State the blood parasite species.
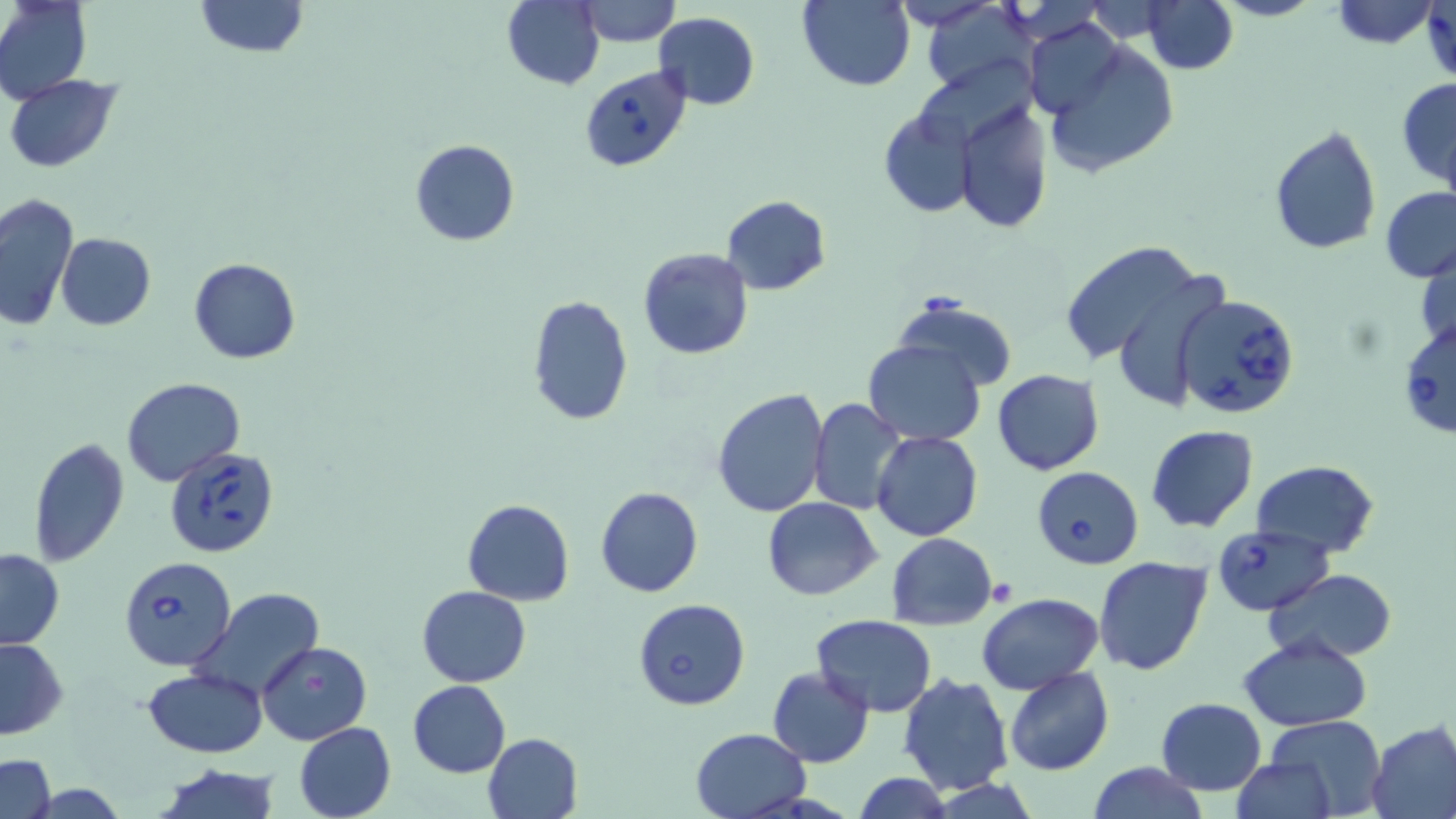

Babesia divergens.

Approximate bounding boxes as [x1, y1, x2, y2] in pixels. Uninfected red blood cell locations: [0, 0, 92, 104], [193, 0, 308, 57], [503, 0, 604, 89], [579, 0, 681, 47], [796, 0, 914, 90], [923, 0, 1036, 95], [1332, 1, 1437, 48], [1142, 2, 1238, 74], [653, 12, 760, 110], [1027, 18, 1125, 121], [1037, 31, 1182, 181], [4, 74, 122, 172], [1398, 76, 1456, 189], [955, 97, 1053, 235], [878, 104, 979, 218], [1268, 126, 1382, 254], [411, 139, 520, 247], [1380, 187, 1456, 283], [0, 192, 77, 332], [721, 194, 831, 294], [57, 232, 155, 330], [1058, 241, 1208, 373], [1417, 245, 1455, 354], [637, 247, 754, 360], [187, 257, 301, 364], [526, 293, 633, 429], [890, 296, 1019, 391], [863, 340, 986, 445], [991, 369, 1104, 475], [121, 377, 246, 487], [712, 386, 829, 518], [809, 397, 909, 514], [1145, 424, 1259, 533], [870, 431, 983, 541], [27, 436, 129, 570], [1252, 460, 1380, 557], [595, 486, 704, 598], [762, 496, 884, 601], [463, 498, 574, 605], [885, 532, 998, 630], [0, 548, 63, 649], [1092, 556, 1213, 675], [1265, 568, 1396, 662], [417, 585, 530, 687], [188, 586, 327, 699], [977, 593, 1103, 693], [634, 598, 749, 711], [812, 614, 937, 715], [0, 635, 67, 739], [1237, 635, 1372, 730], [257, 640, 372, 747], [768, 667, 874, 768], [1003, 667, 1114, 776], [142, 669, 268, 757], [898, 671, 1015, 793], [407, 680, 511, 777], [1156, 696, 1266, 795], [1265, 714, 1384, 819], [1366, 721, 1456, 818], [294, 722, 396, 819], [690, 728, 811, 818], [482, 732, 583, 819], [0, 754, 55, 819], [1231, 757, 1336, 817], [1088, 760, 1206, 819], [154, 764, 283, 819], [850, 772, 953, 819]. Babesia divergens-infected red blood cell locations: [583, 65, 693, 172], [1175, 292, 1301, 419], [1397, 315, 1455, 439], [162, 448, 282, 561], [1031, 466, 1144, 569], [1212, 525, 1333, 617], [118, 556, 236, 673]. Thin blood film. Optical microscopy. Image is 1456×819 pixels. 1000x magnification. Single field of view. May-Grünwald-Giemsa-stained preparation.